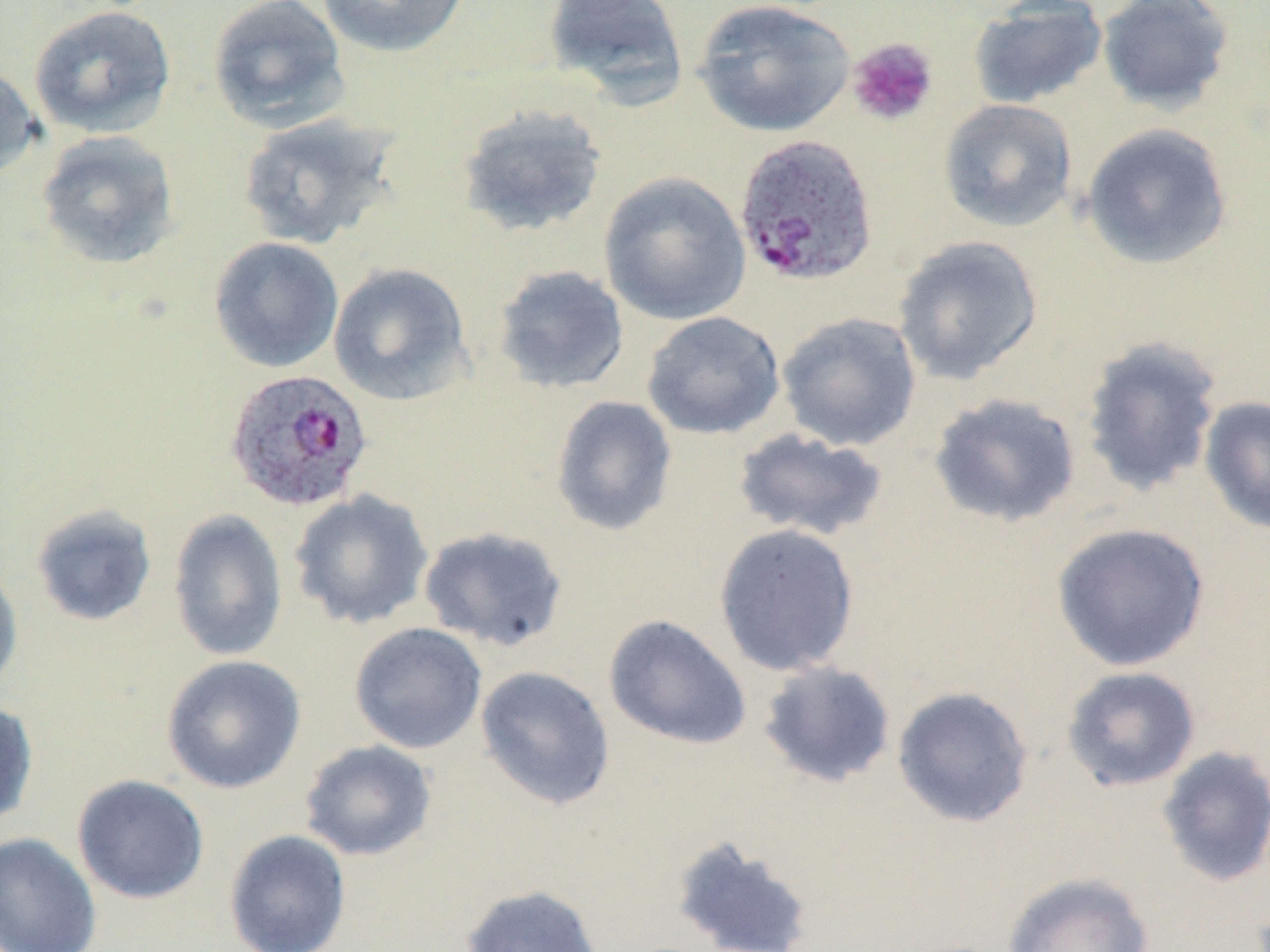

slide-level diagnosis = Plasmodium ovale
modality = optical microscopy
image size = 1270×952 pixels
magnification = 1000x
field of view = one of a larger specimen
preparation = thin blood smear
uninfected red blood cell locations = approximate bounding boxes as named x1/y1/x2/y2 corners in pixels: (x1=207, y1=0, x2=349, y2=132), (x1=315, y1=0, x2=470, y2=58), (x1=541, y1=0, x2=689, y2=107), (x1=692, y1=0, x2=856, y2=138), (x1=1097, y1=0, x2=1235, y2=114), (x1=968, y1=1, x2=1108, y2=109), (x1=28, y1=4, x2=176, y2=139), (x1=0, y1=62, x2=43, y2=183), (x1=938, y1=99, x2=1078, y2=232), (x1=457, y1=104, x2=608, y2=238), (x1=236, y1=112, x2=401, y2=250), (x1=1080, y1=123, x2=1233, y2=270), (x1=35, y1=130, x2=180, y2=270), (x1=598, y1=171, x2=751, y2=325), (x1=893, y1=235, x2=1044, y2=384), (x1=209, y1=237, x2=344, y2=373), (x1=327, y1=262, x2=473, y2=406), (x1=492, y1=265, x2=629, y2=394), (x1=641, y1=311, x2=786, y2=440), (x1=776, y1=312, x2=922, y2=451), (x1=1078, y1=334, x2=1225, y2=498), (x1=928, y1=392, x2=1082, y2=528), (x1=550, y1=395, x2=678, y2=537), (x1=1198, y1=395, x2=1270, y2=536), (x1=733, y1=428, x2=889, y2=542), (x1=289, y1=488, x2=434, y2=630), (x1=30, y1=504, x2=158, y2=627), (x1=168, y1=508, x2=288, y2=661), (x1=1050, y1=522, x2=1211, y2=672), (x1=713, y1=523, x2=861, y2=677), (x1=418, y1=526, x2=569, y2=652), (x1=0, y1=560, x2=23, y2=697), (x1=603, y1=614, x2=753, y2=750), (x1=349, y1=622, x2=487, y2=754), (x1=161, y1=654, x2=306, y2=795), (x1=757, y1=660, x2=897, y2=789), (x1=475, y1=666, x2=615, y2=810), (x1=1060, y1=666, x2=1201, y2=792), (x1=891, y1=685, x2=1034, y2=828), (x1=0, y1=700, x2=39, y2=828), (x1=299, y1=740, x2=437, y2=861), (x1=1157, y1=746, x2=1270, y2=888), (x1=72, y1=774, x2=210, y2=905), (x1=223, y1=829, x2=352, y2=952), (x1=0, y1=831, x2=103, y2=952), (x1=669, y1=834, x2=816, y2=951), (x1=1001, y1=871, x2=1154, y2=952), (x1=460, y1=884, x2=604, y2=952)
Plasmodium ovale-infected red blood cell locations = approximate bounding boxes as named x1/y1/x2/y2 corners in pixels: (x1=733, y1=134, x2=879, y2=287), (x1=223, y1=368, x2=373, y2=513)
stain = May-Grünwald-Giemsa
platelet locations = approximate bounding boxes as named x1/y1/x2/y2 corners in pixels: (x1=846, y1=37, x2=939, y2=126)